Assess this cell for malaria.
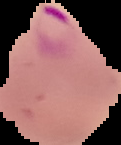

Parasitized.

image_size: 121×145 pixels
preparation: thin blood film
image_type: segmented cell region on a black background